Outline every parasitised red blood cell, every trophozoite, every gametocyte, every leukocyte, and every artifact (platelet-like body, stain precipitate, or debris).
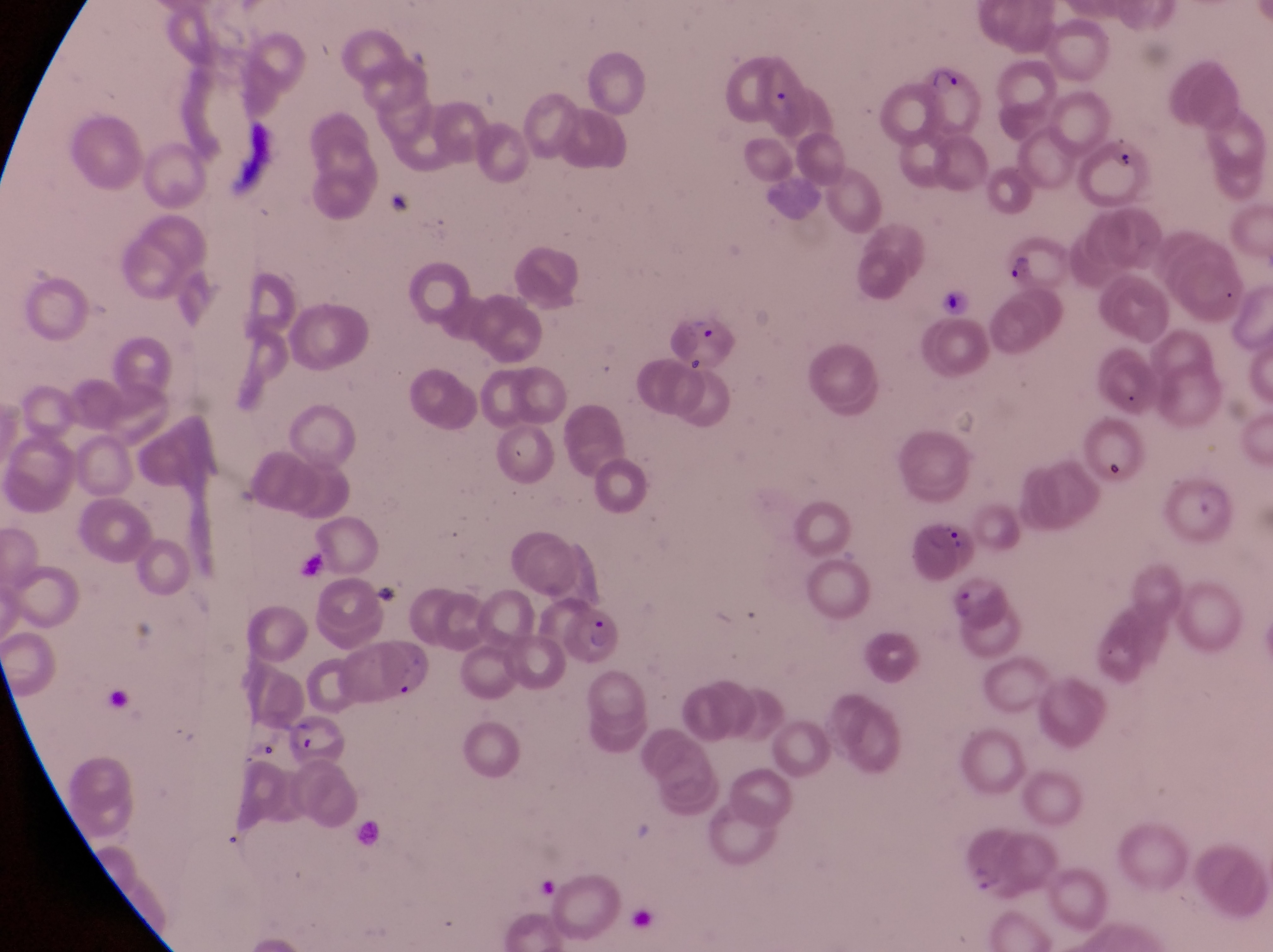
Approximate bounding boxes as [left, top, right, bottom] in pixels.
Parasitised red blood cells: [911, 53, 985, 140], [1078, 130, 1155, 205], [1001, 235, 1071, 293], [662, 309, 739, 372], [914, 512, 977, 580], [562, 604, 632, 672], [287, 717, 352, 769].
No leukocytes observed.
Artifacts (platelet-like body, stain precipitate, or debris): [380, 182, 422, 215], [936, 282, 975, 327].

Thin blood film. Single field of view. Image is 1273×952 pixels. Photographed through the eyepiece of an Olympus CX-23 microscope with a smartphone camera. Sample from Uganda. Magnification of 1000x.